Locate every blood parasite and identify its species.
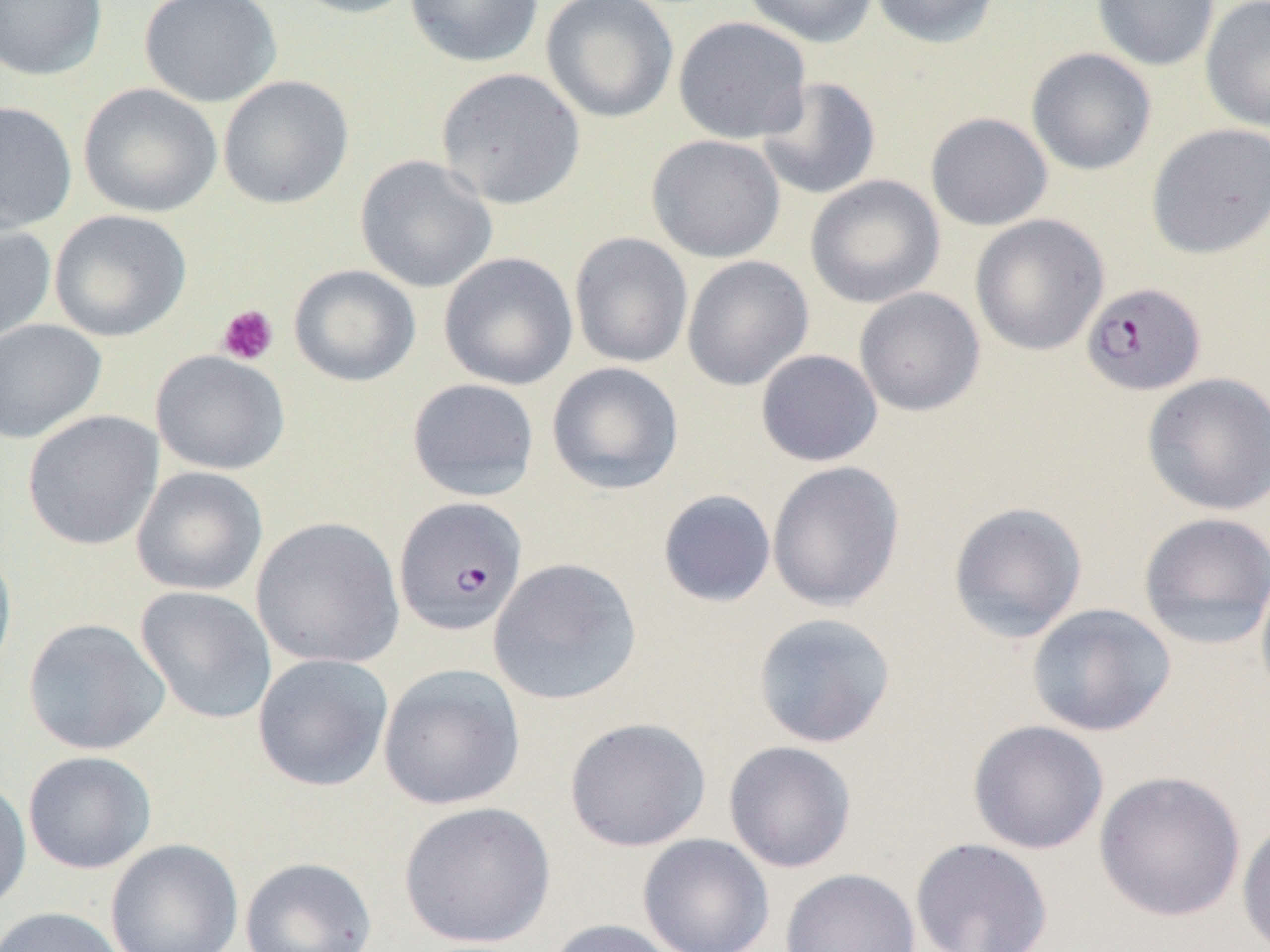
Approximate bounding boxes as (x1, y1, x2, y2) in pixels.
Plasmodium falciparum-infected red blood cells: (1080, 281, 1207, 395), (393, 496, 529, 637).
No Plasmodium ovale, Plasmodium malariae, Plasmodium vivax, Babesia divergens, or Trypanosoma brucei observed.

Uninfected red blood cell locations: (0, 0, 108, 81), (139, 0, 282, 108), (285, 0, 423, 19), (404, 0, 544, 67), (540, 0, 679, 123), (742, 0, 879, 48), (870, 0, 1001, 49), (1092, 0, 1220, 71), (1200, 0, 1270, 133), (672, 16, 812, 145), (1026, 47, 1157, 176), (436, 67, 586, 210), (217, 75, 354, 210), (755, 77, 881, 200), (78, 82, 222, 217), (0, 101, 78, 235), (924, 112, 1053, 231), (1146, 123, 1270, 259), (646, 134, 787, 263), (354, 155, 498, 294), (805, 175, 946, 309), (49, 209, 191, 342), (969, 214, 1110, 356), (0, 221, 56, 349), (568, 232, 694, 369), (438, 252, 578, 390), (681, 255, 814, 391), (288, 264, 421, 387), (853, 287, 985, 416), (0, 318, 107, 444), (755, 349, 883, 467), (150, 350, 290, 475), (546, 361, 685, 496), (1141, 372, 1270, 516), (406, 377, 540, 501), (22, 410, 163, 550), (766, 460, 906, 612), (130, 466, 268, 597), (657, 489, 777, 608), (948, 501, 1088, 642), (1137, 511, 1270, 650), (250, 516, 405, 669), (0, 541, 17, 683), (488, 557, 643, 706), (1255, 567, 1270, 709), (135, 585, 277, 724), (1026, 602, 1177, 737), (752, 612, 897, 748), (22, 618, 170, 756), (252, 653, 394, 792), (377, 664, 526, 811), (564, 716, 712, 852), (967, 719, 1109, 855), (723, 740, 857, 873), (22, 751, 157, 874), (1093, 769, 1247, 922), (0, 775, 32, 916), (398, 801, 556, 949), (1236, 816, 1270, 952), (637, 833, 774, 952), (909, 836, 1054, 952), (104, 838, 244, 952), (240, 856, 377, 951), (779, 867, 921, 952), (0, 906, 128, 952), (543, 918, 685, 952). Platelet locations: (216, 304, 279, 365). Slide-level diagnosis: Plasmodium falciparum. One field of a larger specimen. Captured at 1000x magnification. Image is 1270×952 pixels. Optical microscopy. Thin blood film.